Give the position of every Plasmodium parasite visible.
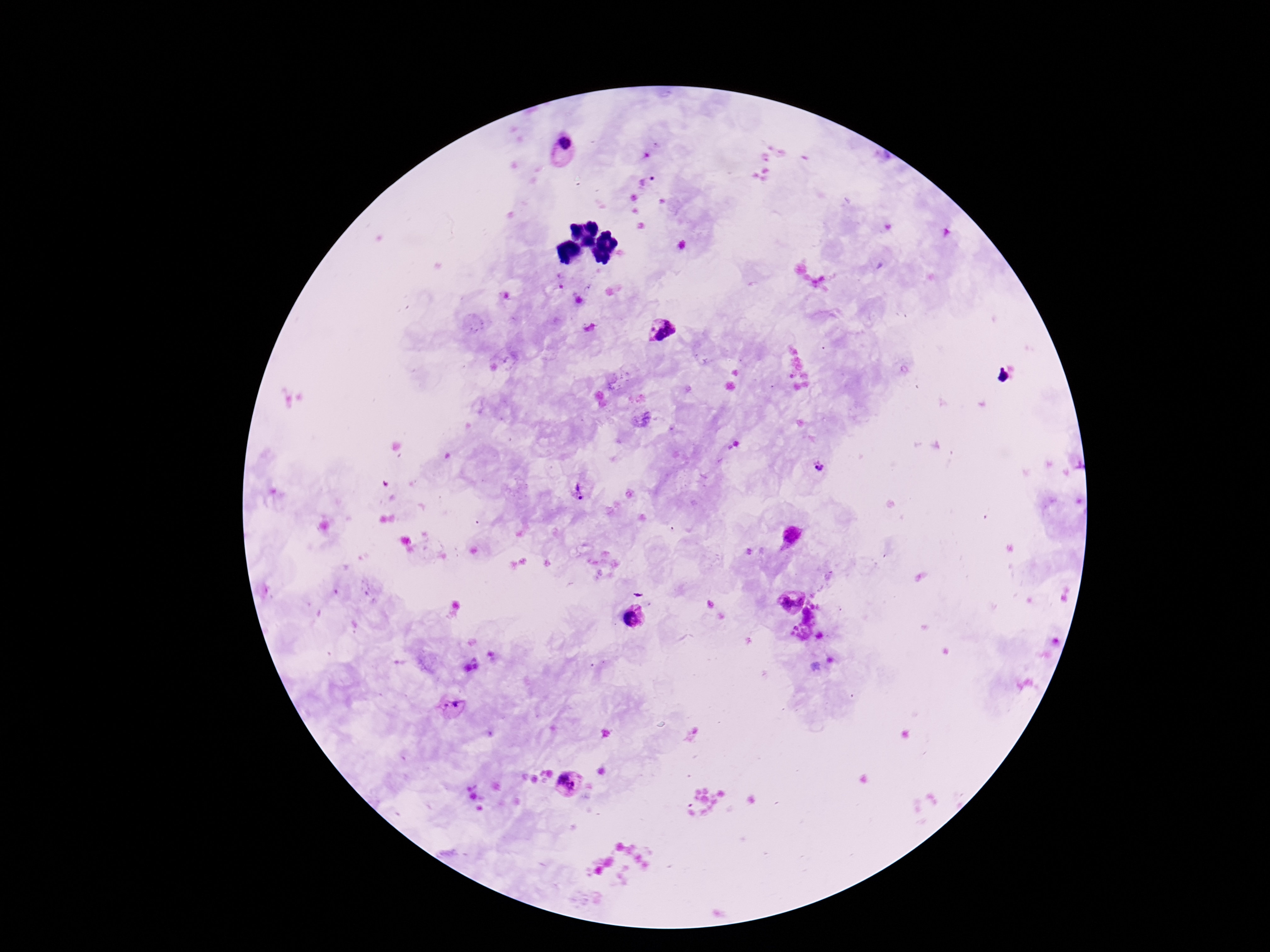
Approximate centers as [x, y] in pixels.
Plasmodium parasites: [564, 144], [646, 181], [662, 332], [641, 419], [818, 468], [577, 490], [792, 536], [789, 598], [633, 618], [454, 707], [566, 785].

magnification: 100x
capture: smartphone camera through the microscope eyepiece
image_size: 1270×952 pixels
stain: Giemsa
patient_malaria_status: positive
preparation: thick blood smear
field_of_view: single